Report the malaria status of this cell.
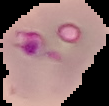

Parasitized.

Summary:
  - Image type: segmented cell region with the area outside set to black
  - Preparation: thin blood smear
  - Image size: 109×106 pixels